Identify the parasite.
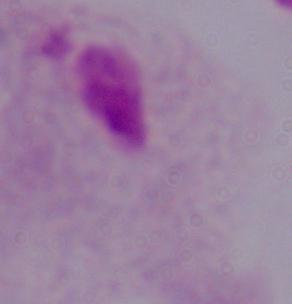
A trichomonad.

Summary:
  - Modality: photomicrograph
  - Magnification: 1000x